Give the position of every Plasmodium parasite.
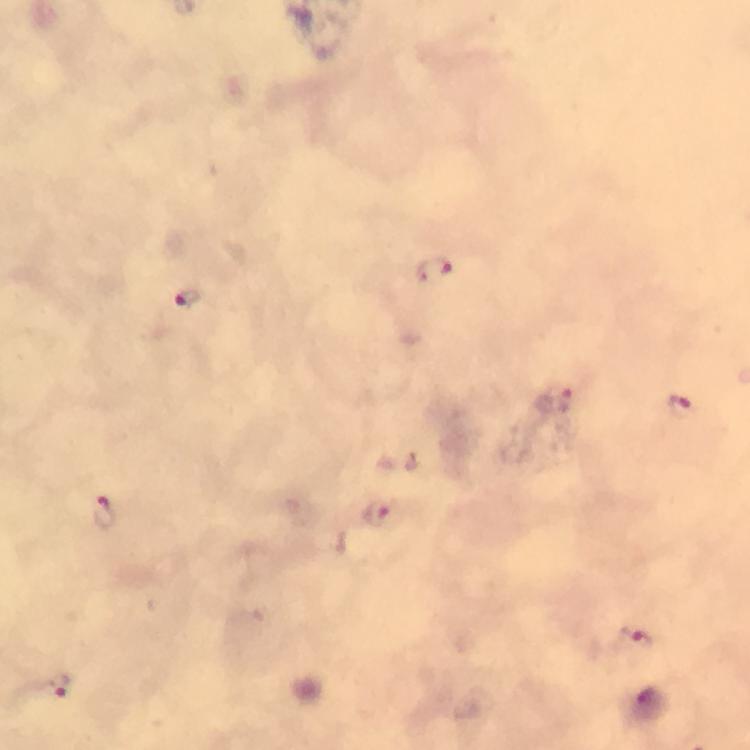
Approximate object centers, in pixels from the top-left corner.
Plasmodium parasites: (x=436, y=269), (x=189, y=296), (x=564, y=399), (x=676, y=404), (x=104, y=512), (x=376, y=515), (x=637, y=639), (x=58, y=685).

Summary:
  - Preparation: thick smear
  - Image size: 750×750 pixels
  - Context: from a malaria diagnostic workup
  - Magnification: 100x
  - Capture: smartphone camera through the microscope
  - Immersion oil: used
  - Cropped from: one field of view
  - Stain: Giemsa